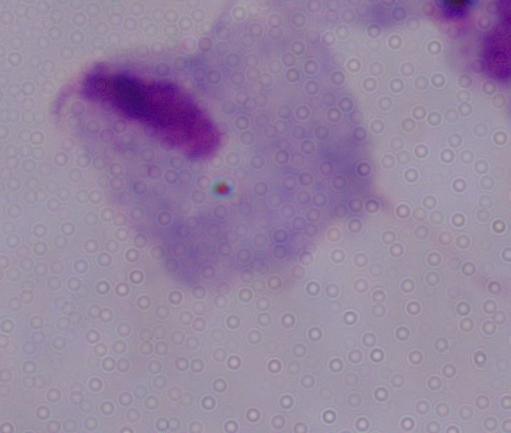

Captured at 1000x magnification. Micrograph. A trichomonad is seen.